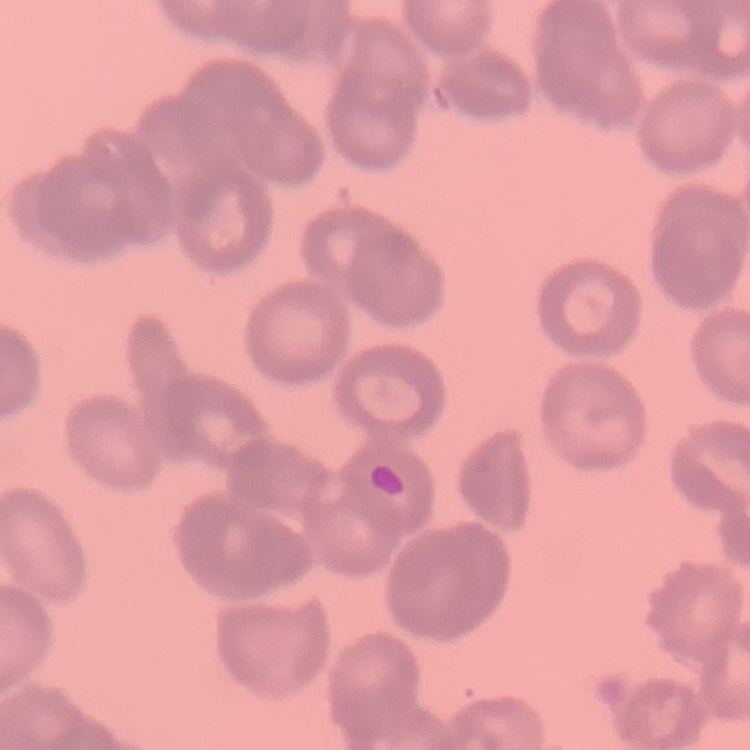 The red blood cells show rouleaux formation. Field's or Giemsa stain. One tile cut from a larger photomicrograph. Thin blood film.